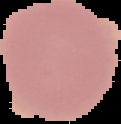
Summary:
  - Image type: segmented cell region with the area outside set to black
  - Image size: 121×124 pixels
  - Malaria status: uninfected
  - Preparation: thin blood film